Assess this cell for malaria.
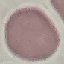

Uninfected.

Giemsa-stained preparation. Photographed with a smartphone camera at the microscope eyepiece. Cell patch, automatically extracted from a larger field of view and resized to 64 × 64 pixels. Thin smear of blood.